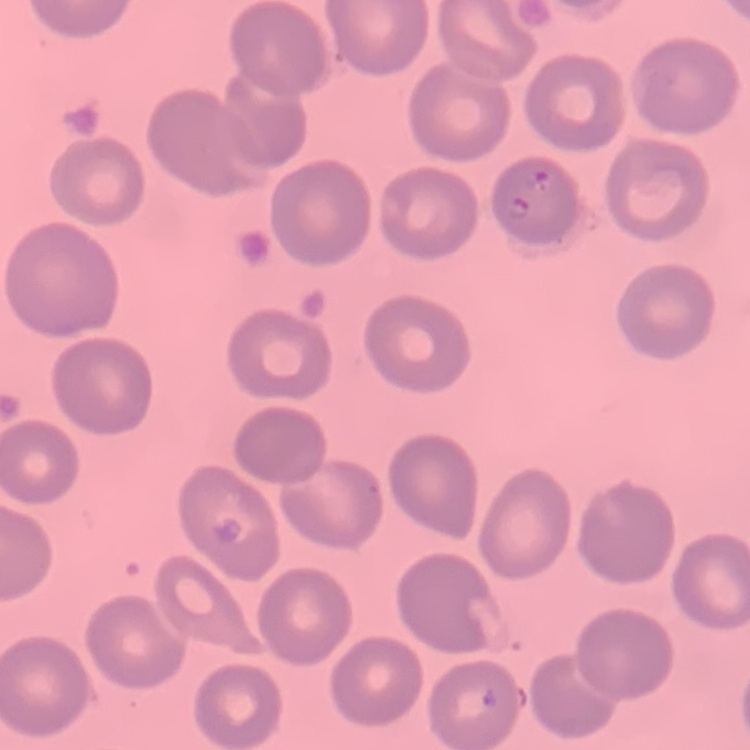

Summary:
  - Erythrocyte morphology: no rouleaux formation
  - Stain: Field's or Giemsa
  - Image type: square crop of a larger photomicrograph
  - Preparation: thin blood smear